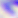
modality = photomicrograph
magnification = 400x
identification = Toxoplasma gondii